Outline each blood parasite and name the species.
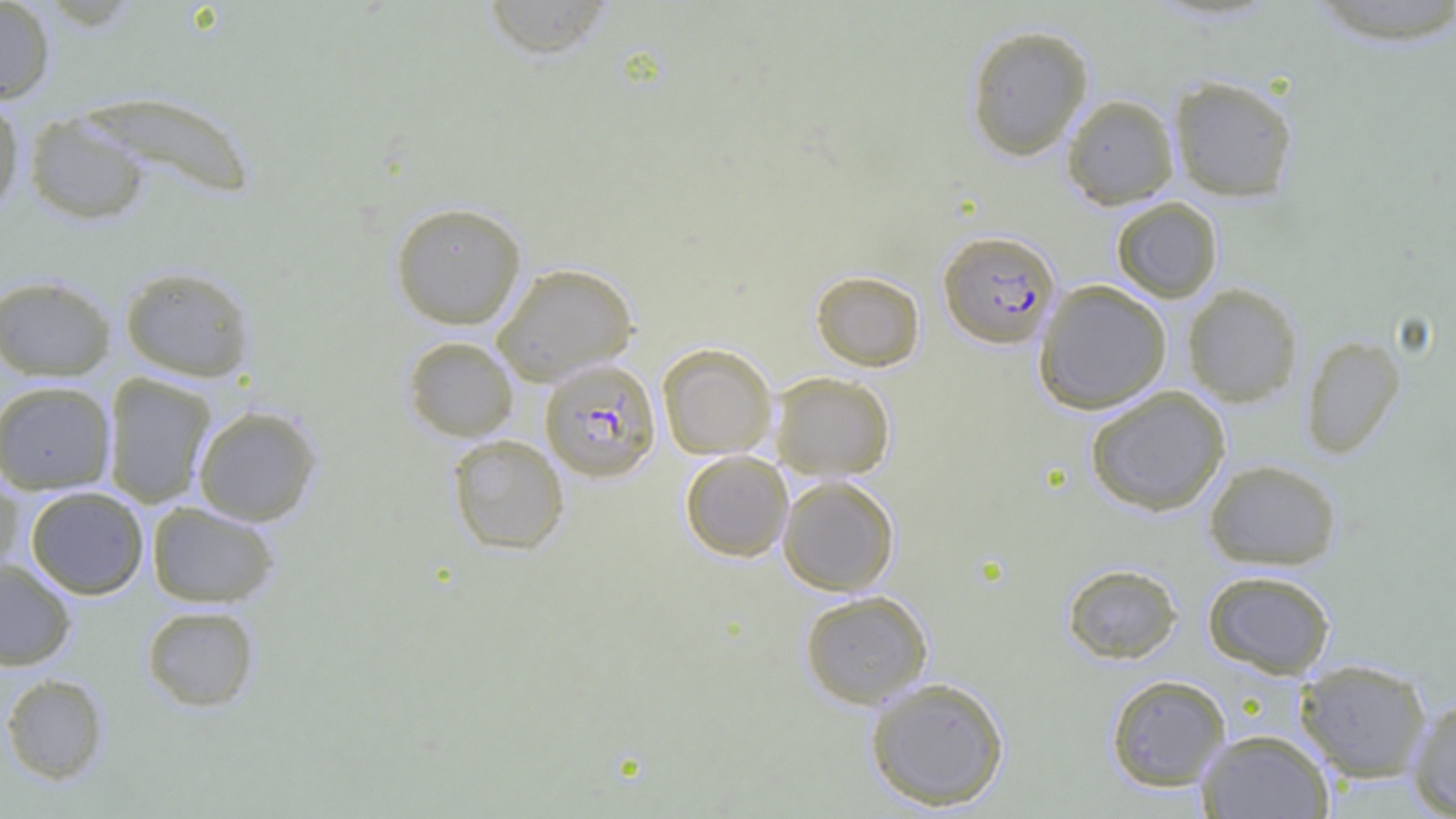

Approximate bounding boxes as named x1/y1/x2/y2 corners in pixels.
Plasmodium falciparum-infected red blood cells: (x1=938, y1=229, x2=1061, y2=348), (x1=539, y1=359, x2=661, y2=482).
No Plasmodium ovale, Plasmodium malariae, Plasmodium vivax, Babesia divergens, or Trypanosoma brucei observed.

slide_level_diagnosis: Plasmodium falciparum
field_of_view: one of a larger specimen
modality: light microscopy
image_size: 1456×819 pixels
magnification: 1000x
uninfected_red_blood_cell_locations: 'approximate bounding boxes as named x1/y1/x2/y2 corners in pixels: (x1=0, y1=0, x2=56, y2=104), (x1=480, y1=0, x2=618, y2=59), (x1=1296, y1=1, x2=1456, y2=48), (x1=964, y1=24, x2=1094, y2=161), (x1=1167, y1=74, x2=1299, y2=203), (x1=75, y1=89, x2=258, y2=200), (x1=1061, y1=94, x2=1179, y2=210), (x1=0, y1=95, x2=26, y2=217), (x1=24, y1=111, x2=150, y2=224), (x1=1111, y1=197, x2=1223, y2=303), (x1=389, y1=200, x2=527, y2=329), (x1=492, y1=262, x2=639, y2=385), (x1=119, y1=264, x2=256, y2=382), (x1=811, y1=270, x2=926, y2=372), (x1=0, y1=274, x2=117, y2=381), (x1=1033, y1=279, x2=1172, y2=414), (x1=1182, y1=283, x2=1303, y2=407), (x1=1300, y1=334, x2=1406, y2=459), (x1=402, y1=335, x2=519, y2=442), (x1=657, y1=342, x2=778, y2=460), (x1=770, y1=371, x2=896, y2=480), (x1=102, y1=373, x2=217, y2=508), (x1=0, y1=380, x2=117, y2=494), (x1=1084, y1=386, x2=1231, y2=516), (x1=191, y1=405, x2=322, y2=526), (x1=446, y1=434, x2=570, y2=555), (x1=680, y1=450, x2=794, y2=562), (x1=1203, y1=458, x2=1342, y2=571), (x1=0, y1=473, x2=23, y2=581), (x1=777, y1=475, x2=900, y2=596), (x1=24, y1=486, x2=149, y2=600), (x1=147, y1=501, x2=280, y2=608), (x1=0, y1=558, x2=77, y2=671), (x1=1062, y1=562, x2=1183, y2=664), (x1=1202, y1=569, x2=1336, y2=678), (x1=798, y1=589, x2=934, y2=709), (x1=141, y1=604, x2=260, y2=712), (x1=1294, y1=659, x2=1433, y2=783), (x1=1, y1=673, x2=110, y2=785), (x1=1105, y1=674, x2=1231, y2=792), (x1=864, y1=676, x2=1010, y2=811), (x1=1406, y1=695, x2=1456, y2=817), (x1=1196, y1=728, x2=1334, y2=818)'
preparation: thin blood smear